Give the extent of all uninfected red blood cells.
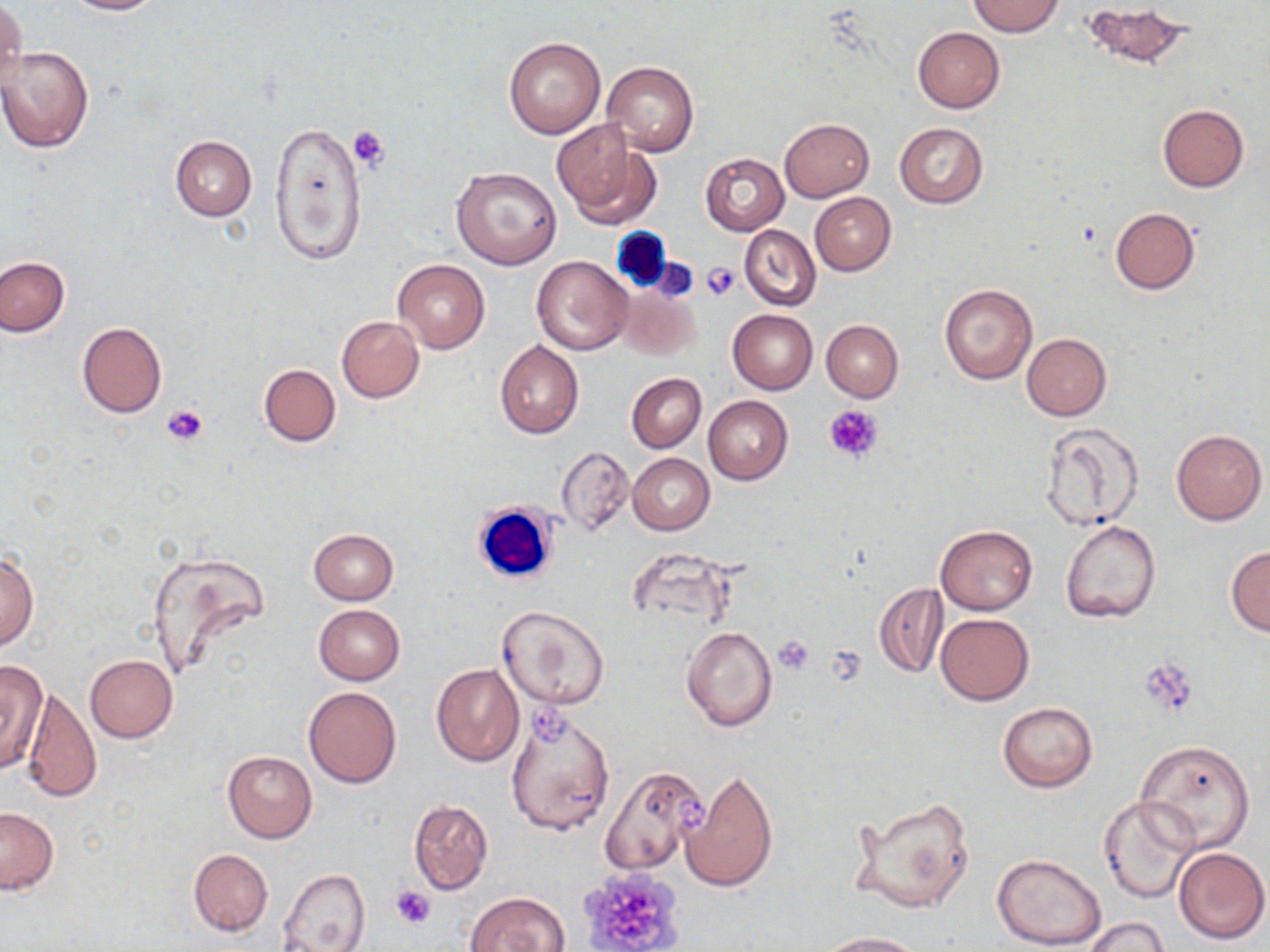

Approximate bounding boxes as named x1/y1/x2/y2 corners in pixels.
Uninfected red blood cells: (x1=63, y1=0, x2=165, y2=15), (x1=968, y1=1, x2=1063, y2=37), (x1=1083, y1=1, x2=1194, y2=68), (x1=1, y1=2, x2=26, y2=94), (x1=911, y1=26, x2=1005, y2=113), (x1=503, y1=37, x2=606, y2=140), (x1=1, y1=45, x2=94, y2=153), (x1=601, y1=60, x2=699, y2=156), (x1=1157, y1=104, x2=1249, y2=192), (x1=780, y1=118, x2=873, y2=201), (x1=551, y1=119, x2=659, y2=225), (x1=269, y1=120, x2=368, y2=268), (x1=894, y1=122, x2=988, y2=209), (x1=169, y1=135, x2=257, y2=221), (x1=700, y1=153, x2=789, y2=235), (x1=450, y1=166, x2=562, y2=271), (x1=810, y1=192, x2=896, y2=276), (x1=1109, y1=207, x2=1200, y2=294), (x1=739, y1=225, x2=820, y2=311), (x1=1, y1=255, x2=68, y2=337), (x1=532, y1=256, x2=632, y2=355), (x1=392, y1=260, x2=489, y2=352), (x1=938, y1=284, x2=1037, y2=384), (x1=617, y1=285, x2=702, y2=362), (x1=727, y1=310, x2=818, y2=394), (x1=336, y1=316, x2=425, y2=403), (x1=821, y1=320, x2=903, y2=402), (x1=76, y1=321, x2=168, y2=418), (x1=1022, y1=333, x2=1112, y2=421), (x1=494, y1=340, x2=585, y2=439), (x1=258, y1=364, x2=340, y2=448), (x1=625, y1=373, x2=706, y2=452), (x1=704, y1=396, x2=793, y2=485), (x1=1039, y1=422, x2=1145, y2=532), (x1=1171, y1=429, x2=1266, y2=525), (x1=555, y1=446, x2=633, y2=537), (x1=628, y1=453, x2=714, y2=535), (x1=1060, y1=521, x2=1161, y2=623), (x1=936, y1=524, x2=1038, y2=614), (x1=309, y1=529, x2=399, y2=604), (x1=1226, y1=546, x2=1270, y2=636), (x1=146, y1=549, x2=270, y2=676), (x1=0, y1=550, x2=38, y2=652), (x1=873, y1=583, x2=947, y2=677), (x1=313, y1=604, x2=406, y2=684), (x1=498, y1=606, x2=608, y2=711), (x1=936, y1=614, x2=1033, y2=705), (x1=681, y1=624, x2=777, y2=732), (x1=86, y1=655, x2=177, y2=742), (x1=0, y1=659, x2=47, y2=776), (x1=432, y1=663, x2=524, y2=767), (x1=304, y1=685, x2=402, y2=788), (x1=23, y1=687, x2=102, y2=804), (x1=998, y1=702, x2=1096, y2=792), (x1=508, y1=709, x2=615, y2=835), (x1=1137, y1=740, x2=1256, y2=850), (x1=223, y1=750, x2=317, y2=842), (x1=600, y1=765, x2=709, y2=877), (x1=680, y1=768, x2=778, y2=894), (x1=849, y1=793, x2=976, y2=914), (x1=1099, y1=794, x2=1203, y2=905), (x1=408, y1=800, x2=493, y2=894), (x1=0, y1=807, x2=58, y2=894), (x1=1172, y1=846, x2=1269, y2=945), (x1=188, y1=849, x2=274, y2=937), (x1=992, y1=853, x2=1107, y2=950), (x1=278, y1=868, x2=370, y2=951), (x1=465, y1=891, x2=570, y2=952), (x1=1082, y1=916, x2=1168, y2=952), (x1=816, y1=931, x2=924, y2=951).

slide-level diagnosis = negative for blood parasites
magnification = 1000x
preparation = thin blood smear
field of view = one of a larger specimen
stain = May-Grünwald-Giemsa
platelet locations = approximate bounding boxes as named x1/y1/x2/y2 corners in pixels: (x1=350, y1=125, x2=392, y2=170), (x1=649, y1=258, x2=699, y2=301), (x1=701, y1=262, x2=739, y2=301), (x1=163, y1=401, x2=211, y2=447), (x1=824, y1=404, x2=884, y2=463), (x1=774, y1=635, x2=816, y2=676), (x1=826, y1=645, x2=866, y2=683), (x1=1139, y1=661, x2=1200, y2=719), (x1=526, y1=704, x2=576, y2=748), (x1=671, y1=793, x2=711, y2=830), (x1=575, y1=867, x2=686, y2=951), (x1=391, y1=885, x2=435, y2=930)
modality = light microscopy
image size = 1270×952 pixels
white blood cell locations = approximate bounding boxes as named x1/y1/x2/y2 corners in pixels: (x1=613, y1=228, x2=672, y2=298), (x1=472, y1=501, x2=561, y2=586)